State which parasite is depicted.
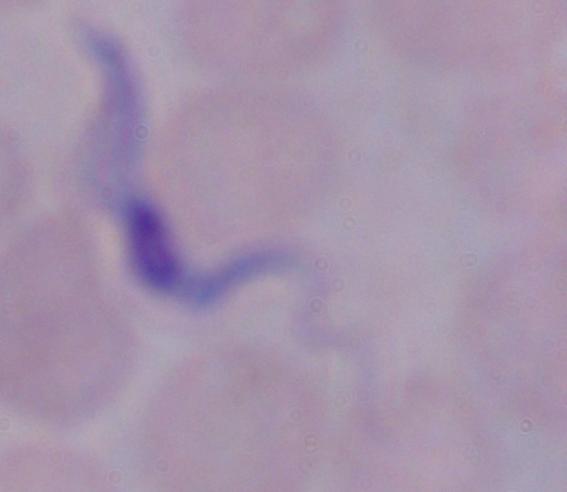

A trypanosome.

Summary:
  - Modality: micrograph
  - Magnification: 1000x